Describe the morphology of the red blood cells.
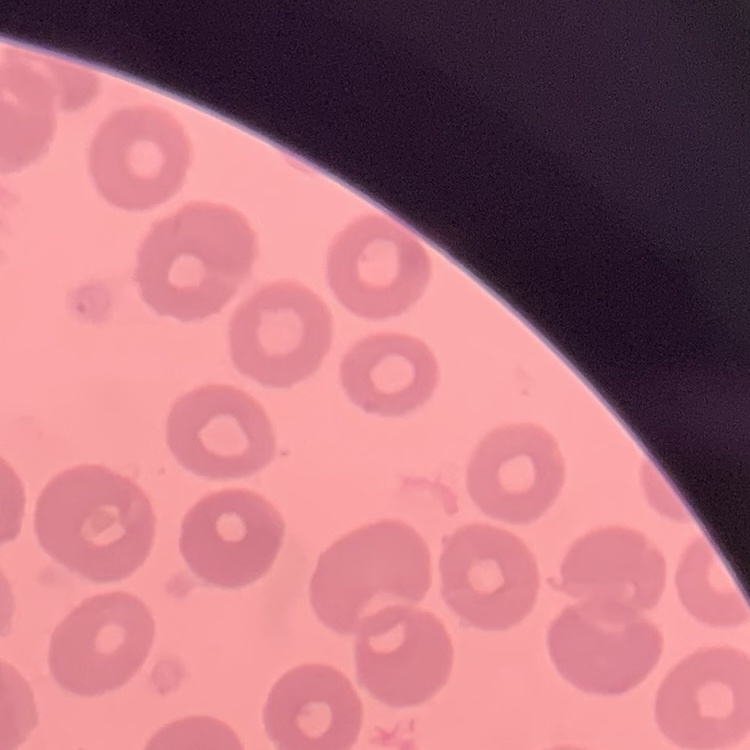
They show no rouleaux formation.

Field's or Giemsa stain. One tile cut from a larger photomicrograph. Thin blood film.